Give the extent of all Plasmodium falciparum-infected red blood cells.
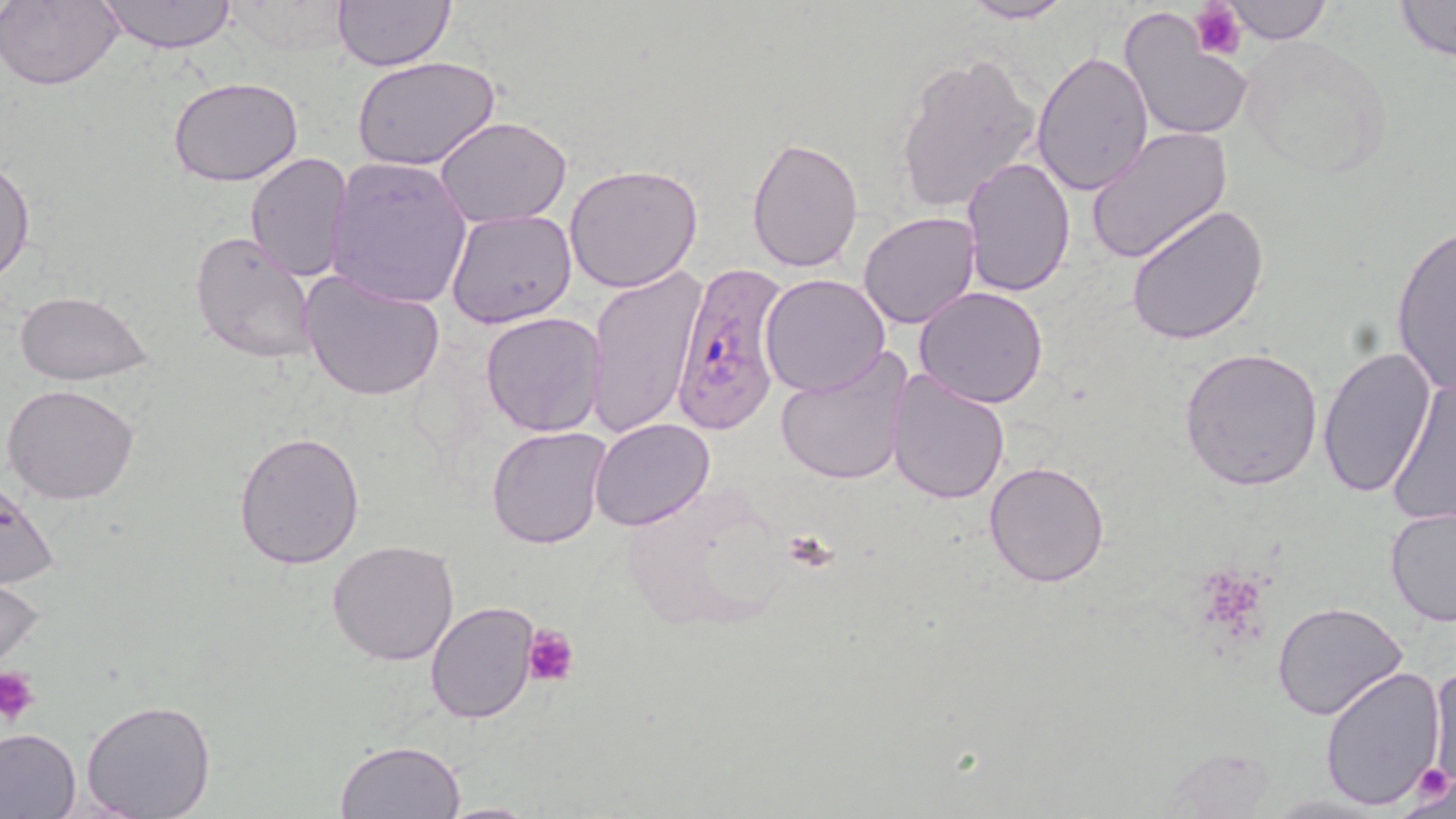
Approximate bounding boxes as (x1, y1, x2, y2) in pixels.
Plasmodium falciparum-infected red blood cells: (670, 259, 788, 435).

Uninfected red blood cell locations: (1, 0, 123, 90), (96, 0, 240, 52), (330, 0, 456, 71), (956, 0, 1076, 23), (1223, 0, 1332, 44), (1390, 0, 1455, 64), (218, 2, 353, 59), (1119, 4, 1253, 143), (1239, 37, 1394, 181), (893, 50, 1043, 213), (1030, 50, 1154, 199), (351, 55, 502, 171), (169, 76, 302, 187), (434, 116, 573, 227), (1084, 127, 1233, 266), (746, 133, 864, 274), (245, 152, 353, 281), (0, 157, 35, 283), (959, 157, 1074, 295), (327, 158, 474, 308), (563, 164, 703, 293), (1126, 202, 1268, 345), (446, 207, 579, 331), (858, 211, 982, 329), (1389, 222, 1455, 396), (189, 230, 320, 364), (587, 268, 707, 438), (298, 269, 447, 403), (759, 273, 891, 397), (914, 287, 1050, 408), (13, 291, 154, 385), (480, 311, 608, 438), (1177, 345, 1324, 491), (1317, 345, 1436, 500), (773, 349, 915, 489), (886, 368, 1012, 504), (1385, 374, 1456, 528), (3, 383, 139, 504), (522, 416, 684, 544), (589, 419, 713, 533), (485, 425, 612, 550), (234, 429, 366, 570), (984, 462, 1110, 587), (0, 479, 61, 590), (1383, 506, 1456, 628), (327, 540, 460, 665), (0, 562, 47, 677), (424, 600, 542, 723), (1272, 602, 1408, 721), (1430, 659, 1456, 791), (1317, 665, 1448, 810), (80, 699, 216, 819), (0, 728, 82, 819), (335, 739, 466, 819), (1155, 745, 1283, 817), (434, 801, 544, 817). Platelet locations: (1191, 2, 1245, 62), (522, 624, 577, 688), (0, 665, 40, 723), (1406, 762, 1455, 808). Slide-level diagnosis: Plasmodium falciparum. May-Grünwald-Giemsa stain. Image is 1456×819 pixels. Captured at 1000x magnification. Single field of view. Light microscopy. Thin blood film.